Identify the parasite.
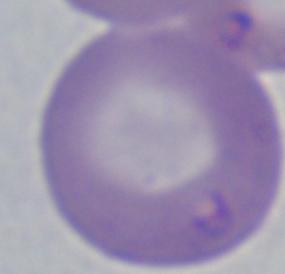

Babesia.

magnification: 1000x
modality: photomicrograph